Describe the morphology of the erythrocytes.
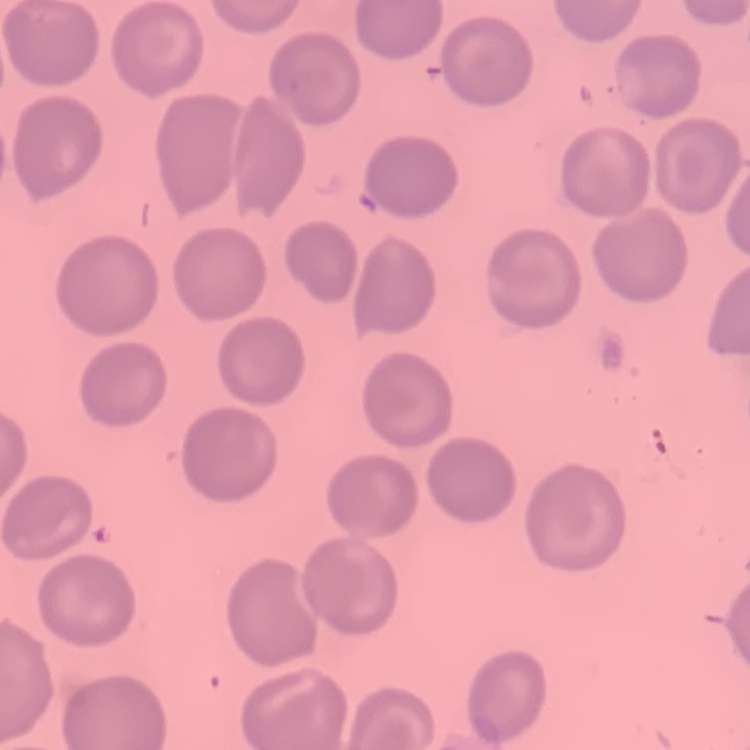

No rouleaux formation.

Summary:
  - Preparation: thin blood film
  - Stain: Field's or Giemsa
  - Image type: one tile cut from a larger photomicrograph